Comment on the morphology of the red blood cells.
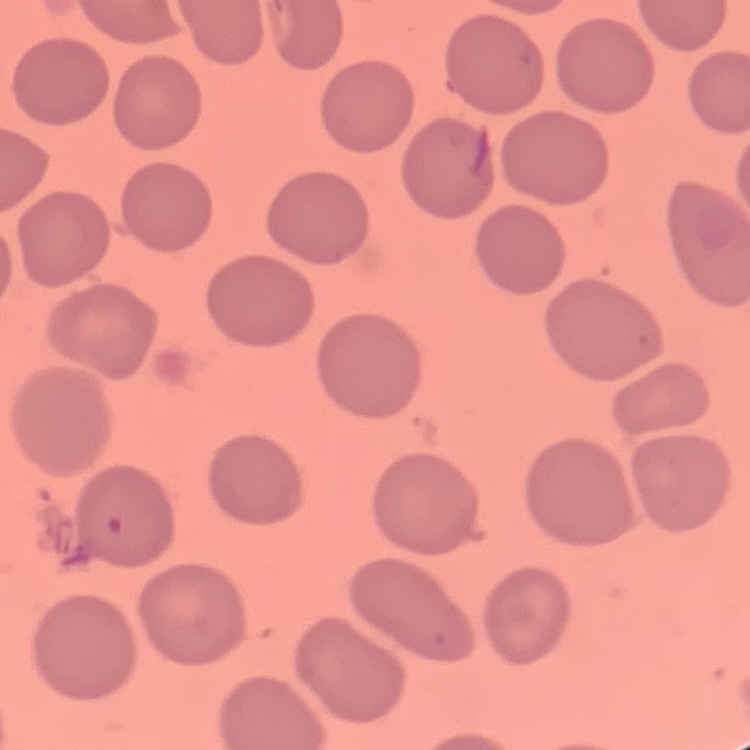
No rouleaux formation.

stain = Field's or Giemsa
preparation = thin blood smear
image type = square crop of a larger photomicrograph